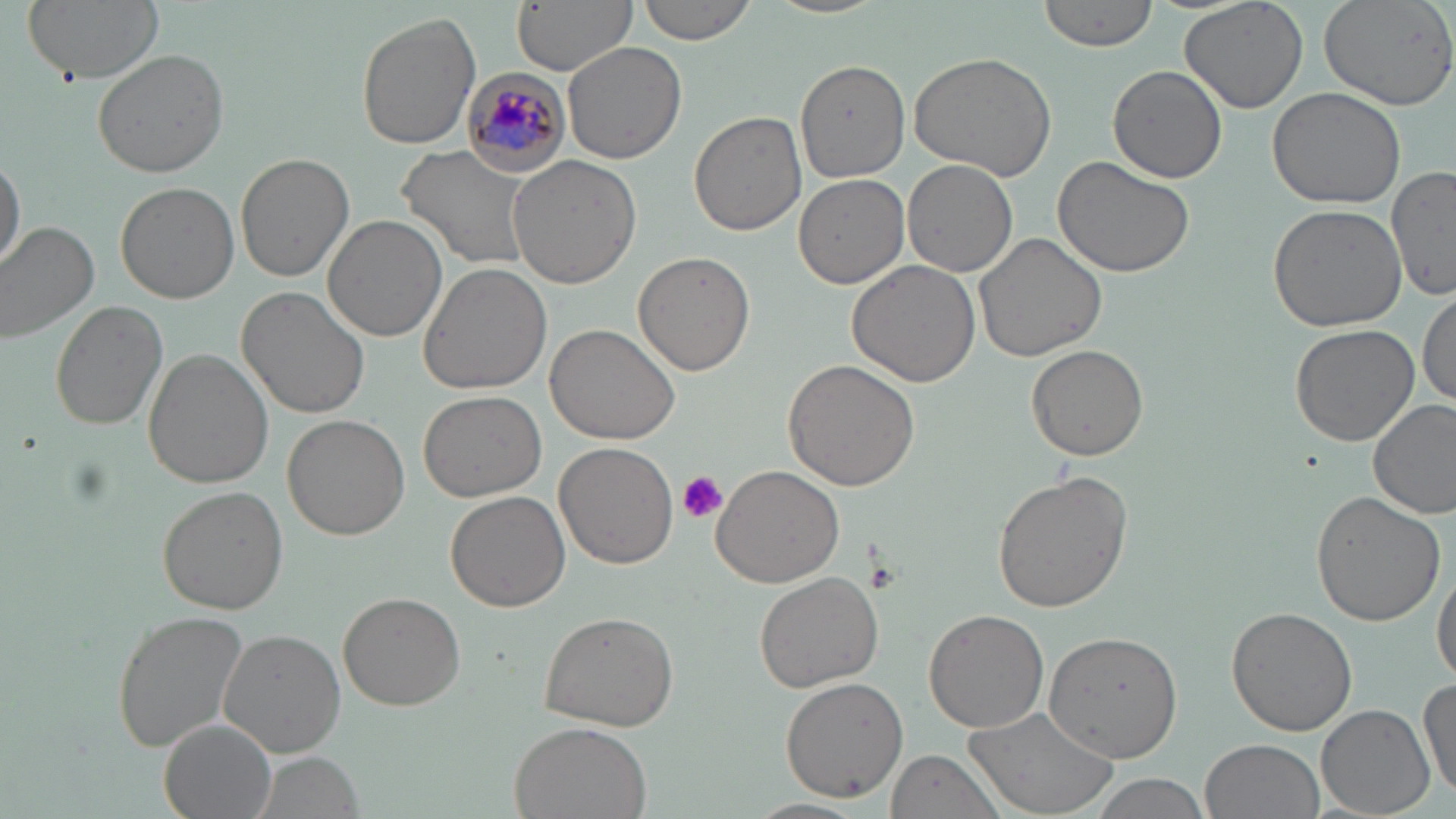

Approximate bounding boxes as (x1, y1, x2, y2) in pixels. Plasmodium malariae-infected red blood cell locations: (462, 70, 569, 175). Platelet locations: (675, 471, 728, 522). Uninfected red blood cell locations: (23, 0, 165, 83), (511, 0, 637, 75), (634, 0, 760, 44), (1038, 0, 1162, 53), (1177, 0, 1308, 113), (1318, 0, 1456, 110), (355, 12, 481, 151), (564, 41, 688, 167), (91, 49, 228, 178), (906, 52, 1057, 179), (796, 59, 910, 181), (1106, 64, 1229, 184), (1268, 85, 1408, 209), (689, 110, 807, 236), (397, 146, 536, 271), (0, 150, 25, 279), (236, 153, 355, 283), (508, 154, 644, 288), (1052, 154, 1196, 277), (903, 159, 1018, 279), (1389, 165, 1456, 303), (794, 174, 910, 290), (115, 181, 239, 303), (1266, 203, 1406, 332), (323, 214, 447, 341), (0, 220, 101, 343), (972, 232, 1107, 362), (633, 251, 756, 376), (848, 259, 983, 388), (418, 263, 553, 394), (1417, 284, 1455, 409), (236, 286, 371, 418), (50, 300, 168, 431), (546, 323, 681, 444), (1289, 324, 1420, 447), (1026, 344, 1147, 461), (143, 351, 273, 488), (783, 359, 920, 492), (418, 391, 548, 502), (1370, 397, 1456, 519), (283, 413, 411, 542), (555, 442, 678, 570), (710, 462, 846, 588), (992, 469, 1134, 613), (156, 486, 289, 615), (444, 489, 570, 612), (1310, 491, 1444, 627), (1431, 560, 1456, 689), (754, 570, 883, 692), (339, 592, 465, 711), (109, 607, 253, 755), (1226, 607, 1357, 736), (538, 608, 682, 732), (924, 610, 1050, 734), (220, 629, 345, 757), (1043, 631, 1186, 761), (1418, 672, 1455, 806), (779, 677, 907, 802), (1317, 704, 1434, 817), (967, 705, 1119, 816), (160, 720, 277, 819), (508, 721, 654, 819), (1201, 738, 1324, 819), (882, 749, 1014, 819), (250, 751, 366, 819), (1086, 774, 1212, 818), (744, 798, 871, 819). Slide-level diagnosis: Plasmodium malariae. Single field of view. May-Grünwald-Giemsa-stained preparation. Thin blood film. Light microscopy. Image is 1456×819 pixels. Captured at 1000x magnification.